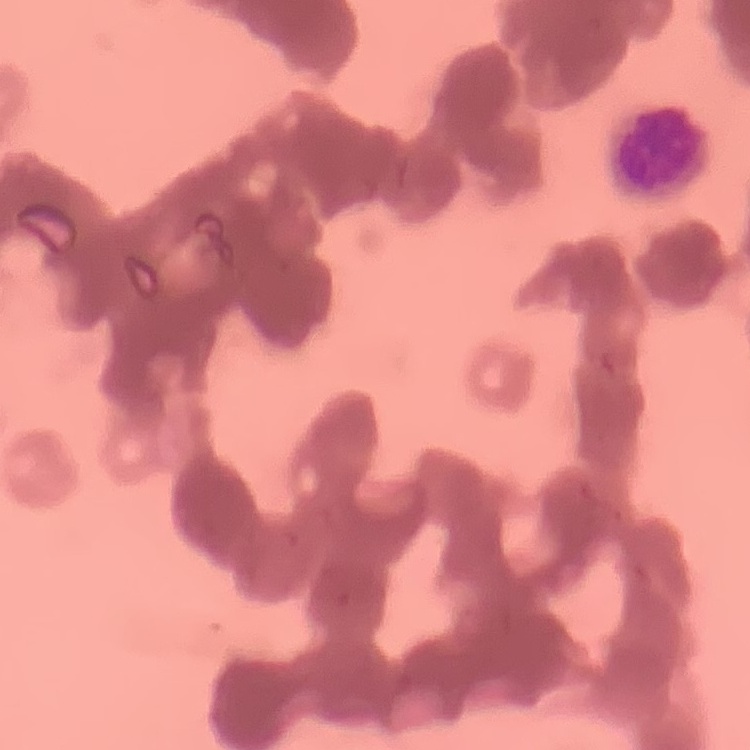

The erythrocytes exhibit rouleaux formation. Thin blood smear. Stained with either Field's or Giemsa. Square crop of a larger photomicrograph.